Report the malaria status of this cell.
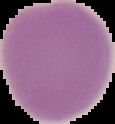
Uninfected.

image type = cell region segmented out of the field of view; surrounding area masked to black
image size = 115×124 pixels
preparation = thin blood smear